Describe the morphology of the erythrocytes.
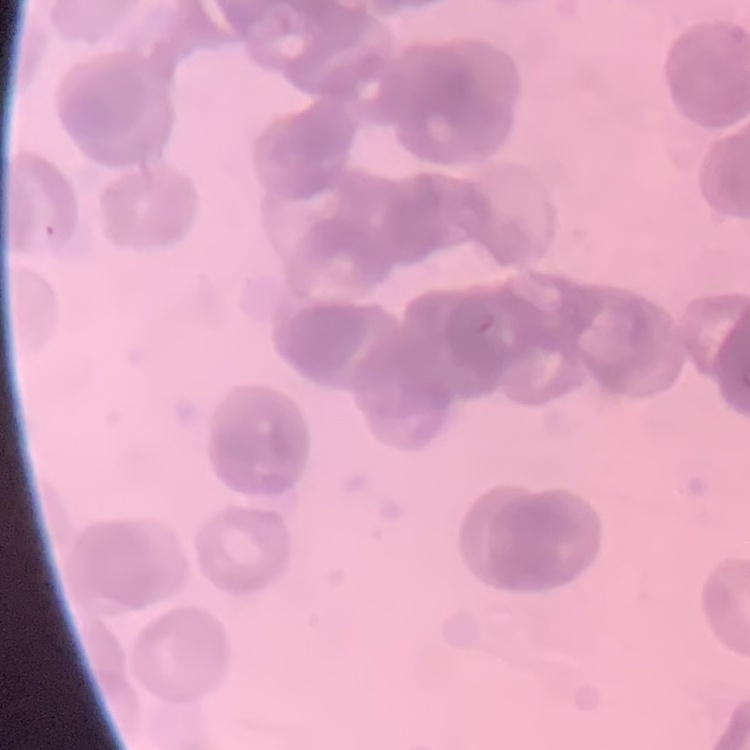
Rouleaux formation.

Summary:
  - Image type: one tile cut from a larger photomicrograph
  - Preparation: thin blood film
  - Stain: Field's or Giemsa